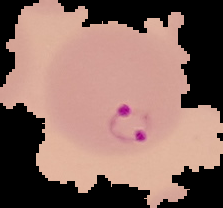

From a thin blood smear. Malaria status: parasitized. Image is 223×208 pixels. Cell region segmented out of the field of view; the surrounding area is masked to black.